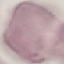 Result: no malaria parasites seen. Thin blood smear. Cell patch, automatically extracted from a larger field of view and resized to 64 × 64 pixels. Acquired by smartphone through the microscope eyepiece. Giemsa stain.